Assess the morphology of the red blood cells.
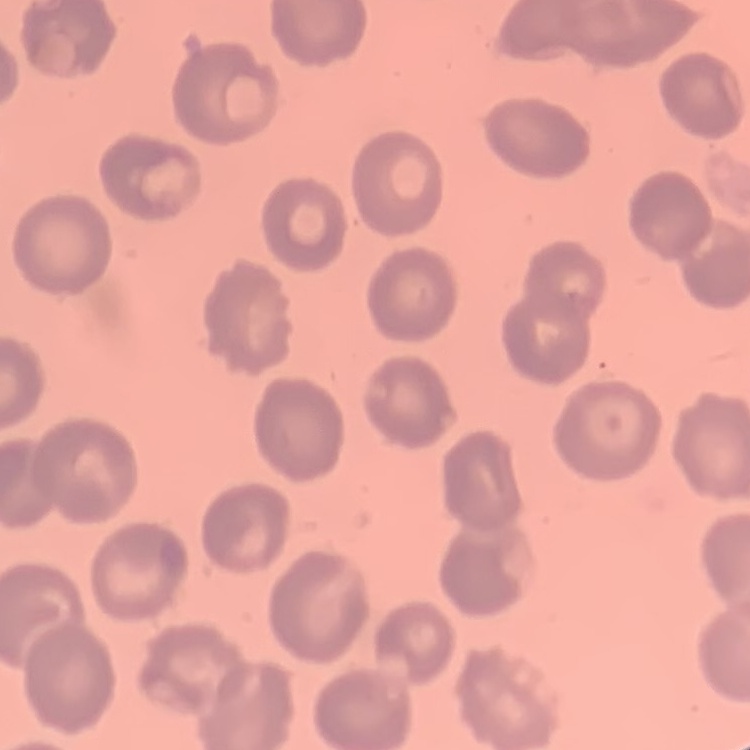

No rouleaux formation.

{
  "image_type": "square crop of a larger photomicrograph",
  "preparation": "thin blood smear",
  "stain": "Field's or Giemsa"
}